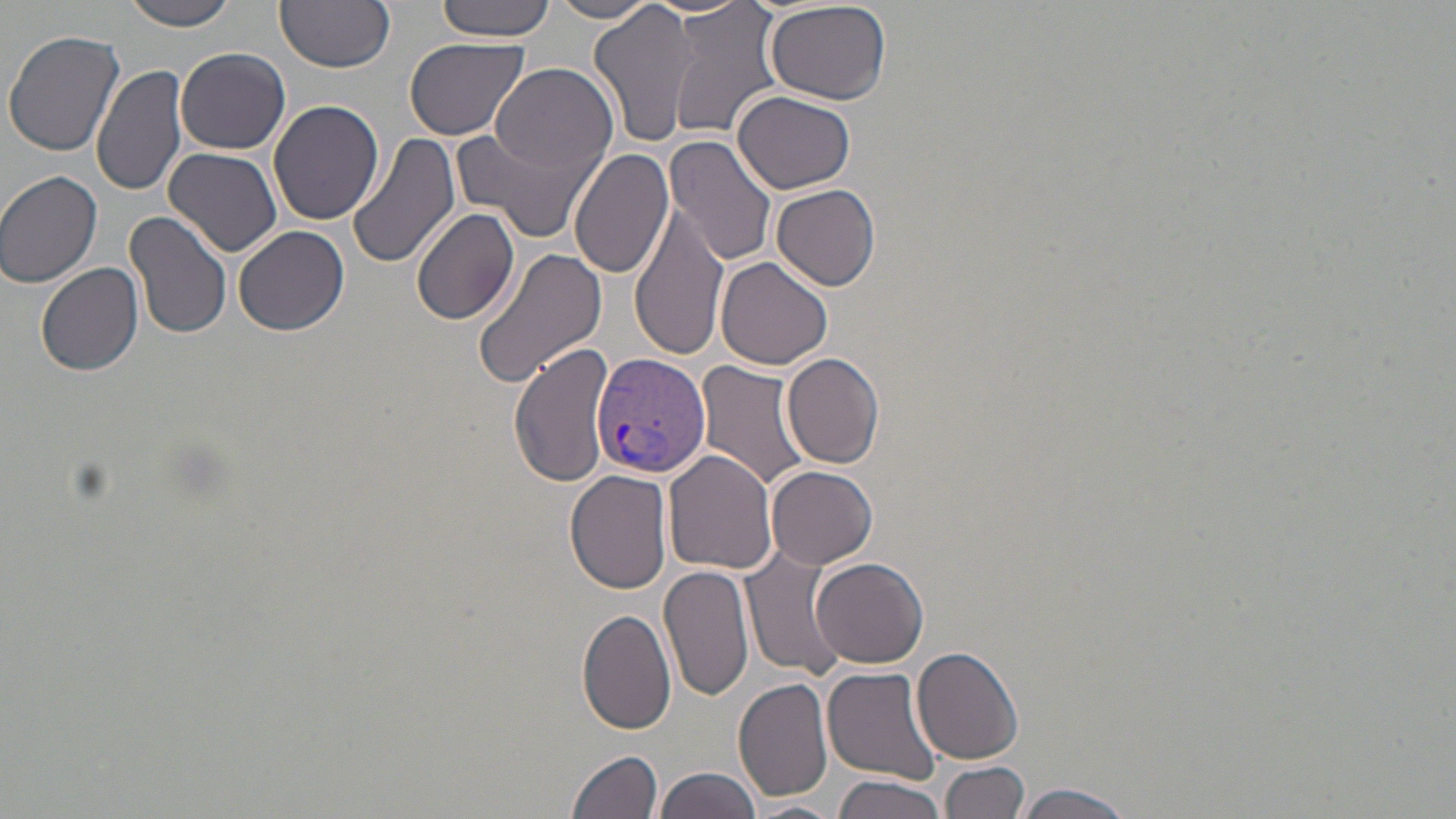

Summary:
  - Coordinate format: approximate bounding boxes as (x1,y1)-(x2,y2) corner pairs in pixels
  - Uninfected red blood cell locations: (119,0)-(242,31), (276,0)-(395,72), (437,0)-(556,40), (548,1)-(659,24), (589,2)-(699,150), (663,2)-(784,139), (764,2)-(895,105), (4,29)-(124,157), (405,37)-(528,140), (175,47)-(290,155), (91,63)-(189,199), (490,63)-(620,178), (734,91)-(856,195), (269,98)-(385,226), (454,122)-(602,245), (349,131)-(461,269), (666,136)-(778,267), (569,146)-(676,280), (162,147)-(284,259), (0,169)-(104,289), (773,184)-(881,291), (631,205)-(730,360), (410,207)-(520,329), (124,209)-(232,342), (233,224)-(350,336), (473,244)-(608,390), (716,254)-(834,369), (36,262)-(144,376), (508,341)-(612,490), (783,352)-(885,468), (694,360)-(810,491), (663,448)-(778,574), (766,466)-(878,569), (565,469)-(675,594), (743,551)-(845,680), (812,557)-(929,669), (660,562)-(752,704), (577,609)-(678,736), (913,646)-(1025,764), (822,665)-(945,786), (733,677)-(834,803), (568,749)-(663,819), (939,759)-(1028,819), (656,766)-(761,819), (832,774)-(949,819), (1017,783)-(1136,819), (741,800)-(844,817)
  - Plasmodium vivax-infected red blood cell locations: (591,353)-(710,479)
  - Slide-level diagnosis: Plasmodium vivax
  - Preparation: thin blood film
  - Modality: optical microscopy
  - Stain: May-Grünwald-Giemsa
  - Field of view: one of a larger specimen
  - Magnification: 1000x
  - Image size: 1456×819 pixels